Locate every malaria parasite.
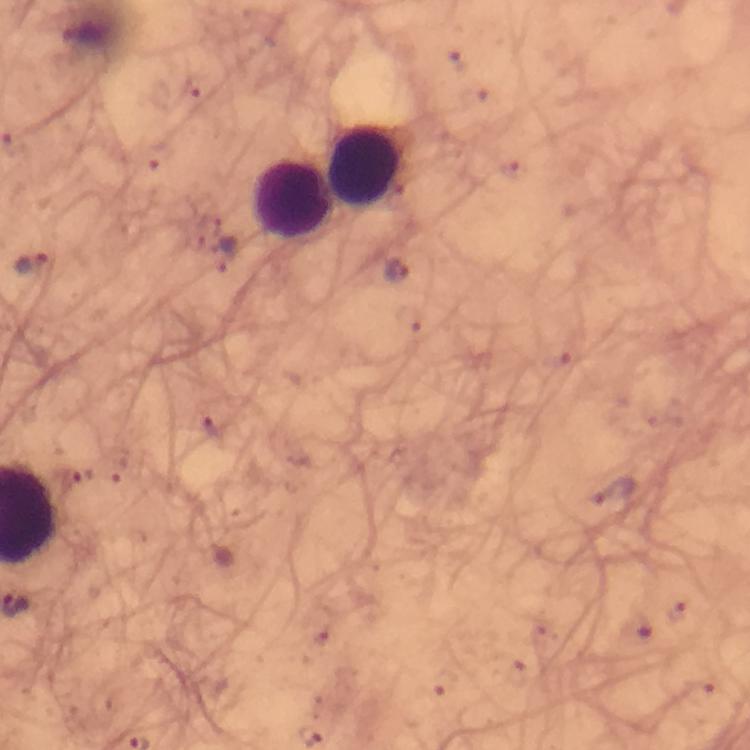

Approximate centers as [x, y] in pixels.
Malaria parasites: [224, 258], [33, 264], [397, 271], [78, 480].

Leukocyte locations: [368, 165], [292, 199]. Image is 750×750 pixels. Thick smear. From a malaria diagnostic workup. Photographed with a smartphone mounted on the microscope. Giemsa-stained preparation. Immersion oil was used. Cropped region of a single field of view. At 100x magnification.